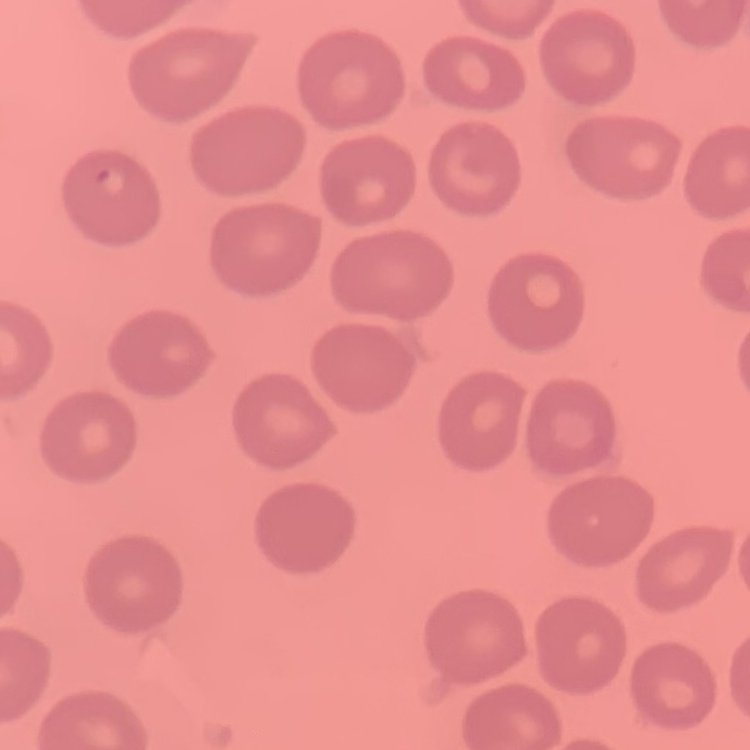

Summary:
  - Erythrocyte morphology: no rouleaux formation
  - Preparation: thin blood film
  - Stain: Field's or Giemsa
  - Image type: square crop of a larger photomicrograph